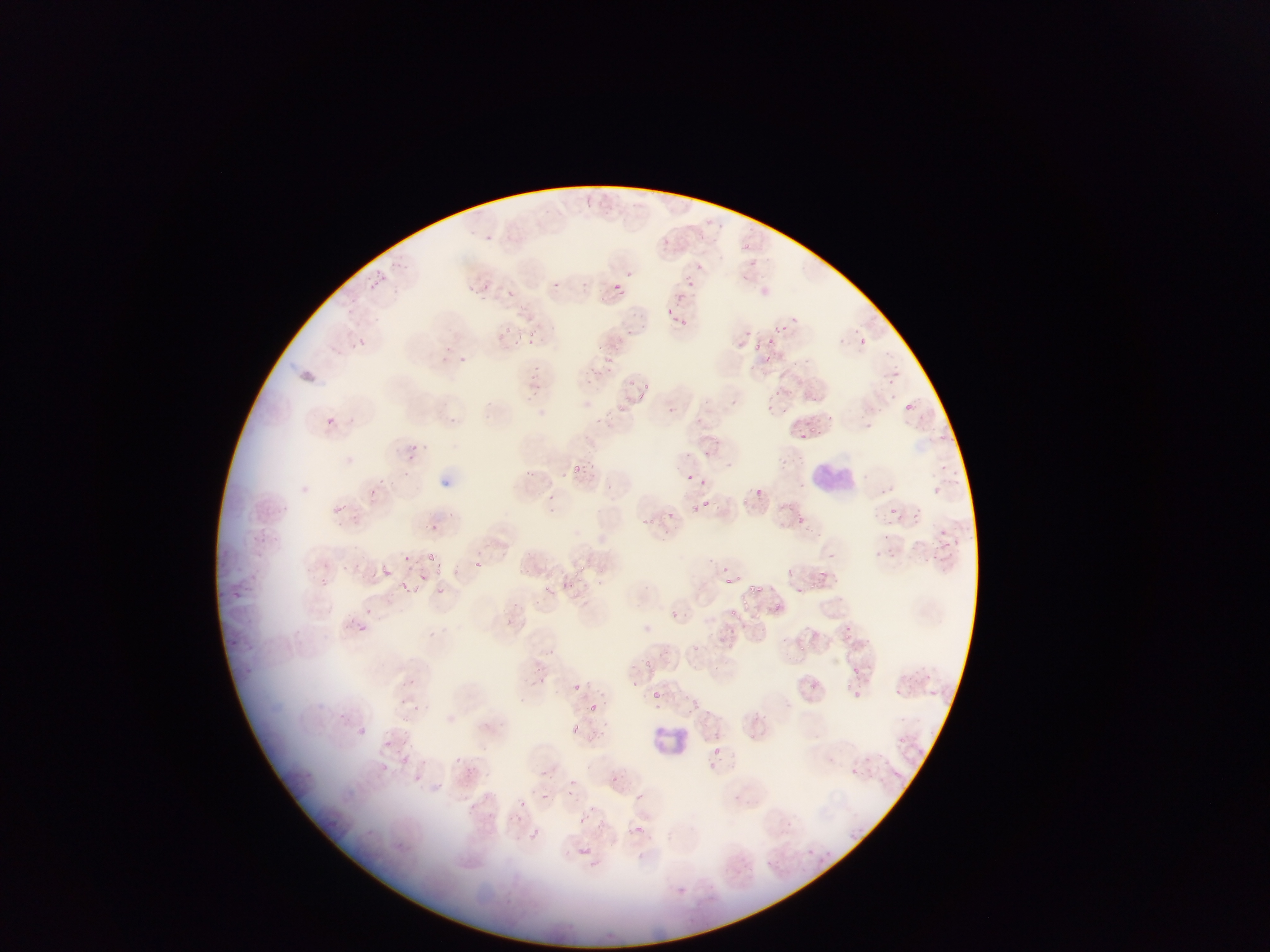
Approximate bounding boxes as {left, top, right, bottom} in pixels. Malaria parasite locations (subset; some below the resolvable size): {482, 233, 494, 243}, {661, 237, 672, 249}, {386, 256, 399, 268}, {694, 261, 705, 271}, {375, 267, 390, 283}, {623, 268, 635, 279}, {363, 278, 376, 296}, {552, 279, 563, 295}, {464, 280, 489, 296}, {677, 280, 692, 297}, {611, 283, 622, 294}, {496, 287, 520, 303}, {514, 303, 538, 321}, {667, 303, 680, 316}, {668, 315, 684, 324}, {777, 318, 795, 332}, {504, 320, 518, 334}, {740, 322, 754, 338}, {623, 324, 639, 338}, {524, 329, 543, 345}, {765, 336, 775, 343}, {355, 337, 366, 348}, {857, 337, 866, 346}, {595, 344, 609, 357}, {880, 346, 892, 359}, {763, 354, 774, 364}, {893, 364, 906, 375}, {883, 374, 894, 385}, {620, 380, 637, 389}, {644, 381, 654, 386}, {775, 386, 783, 393}, {640, 392, 648, 402}, {764, 399, 774, 410}, {905, 399, 913, 409}, {617, 404, 627, 411}, {820, 411, 837, 422}, {323, 416, 337, 428}, {864, 419, 879, 435}, {805, 420, 816, 434}, {799, 435, 810, 446}, {407, 444, 419, 457}, {706, 447, 713, 457}, {570, 462, 595, 478}, {935, 464, 949, 478}, {526, 468, 538, 477}, {407, 469, 418, 483}, {684, 471, 698, 479}, {703, 478, 708, 486}, {373, 480, 393, 491}, {932, 481, 946, 501}, {883, 485, 914, 498}, {756, 487, 767, 497}, {545, 493, 555, 499}, {369, 494, 384, 510}, {703, 495, 711, 505}, {328, 499, 350, 518}, {886, 499, 898, 513}, {692, 504, 703, 516}, {913, 504, 922, 522}, {668, 510, 683, 523}, {794, 511, 805, 521}, {634, 516, 658, 529}, {426, 520, 442, 534}, {878, 531, 891, 544}, {936, 533, 957, 543}, {890, 545, 903, 563}, {824, 547, 837, 557}, {877, 547, 885, 557}, {926, 551, 946, 562}, {404, 553, 419, 567}, {422, 553, 442, 565}, {471, 559, 483, 570}, {784, 563, 800, 576}, {381, 566, 395, 577}, {819, 567, 829, 580}, {414, 573, 431, 586}, {395, 577, 422, 599}, {724, 578, 732, 585}, {749, 580, 768, 596}, {796, 584, 807, 599}, {436, 586, 448, 597}, {738, 594, 752, 605}, {362, 599, 372, 616}, {769, 603, 780, 613}, {668, 607, 687, 626}, {727, 607, 740, 622}, {352, 618, 364, 634}, {842, 621, 852, 632}, {717, 630, 728, 641}, {684, 639, 704, 656}, {644, 656, 657, 669}, {848, 665, 864, 679}, {927, 672, 938, 680}, {405, 675, 424, 686}, {817, 678, 836, 694}, {572, 683, 582, 693}, {852, 687, 863, 698}, {927, 687, 944, 703}, {651, 690, 661, 701}, {944, 692, 960, 706}, {398, 693, 409, 704}, {689, 697, 702, 710}, {580, 698, 604, 717}, {709, 706, 729, 723}, {339, 708, 350, 718}, {356, 724, 373, 739}, {570, 724, 592, 740}, {902, 731, 916, 745}, {380, 738, 396, 748}, {713, 746, 726, 759}, {398, 751, 410, 761}, {863, 753, 876, 765}, {453, 754, 466, 764}, {381, 762, 391, 773}, {853, 765, 867, 779}, {539, 766, 558, 782}, {566, 777, 576, 787}, {560, 787, 573, 800}, {628, 790, 643, 806}, {541, 793, 550, 801}, {516, 798, 535, 812}, {577, 816, 586, 825}, {632, 821, 648, 835}, {523, 827, 543, 846}, {847, 831, 867, 844}, {575, 839, 597, 857}, {804, 846, 817, 856}, {807, 850, 833, 869} | approximate {x, y} pixel centers of objects too small to bound: {757, 342}, {551, 510}. Leukocyte locations: {809, 457, 860, 501}, {655, 721, 702, 761}. One field of view. Image is 1270×952 pixels. Collected in Ghana. Thin blood film. Photographed through a microscope with a mobile-phone camera.